State which cell type is depicted.
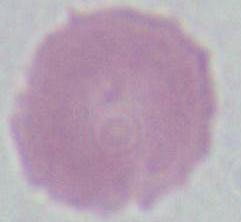
An erythrocyte.

magnification: 1000x
modality: micrograph